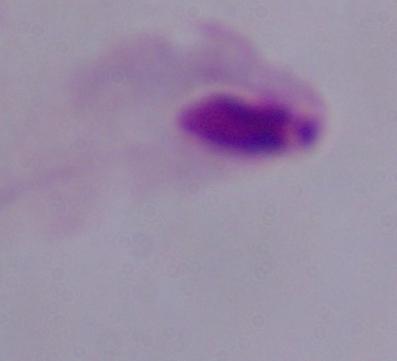

identification = trichomonad
modality = micrograph
magnification = 1000x